Describe the morphology of the red blood cells.
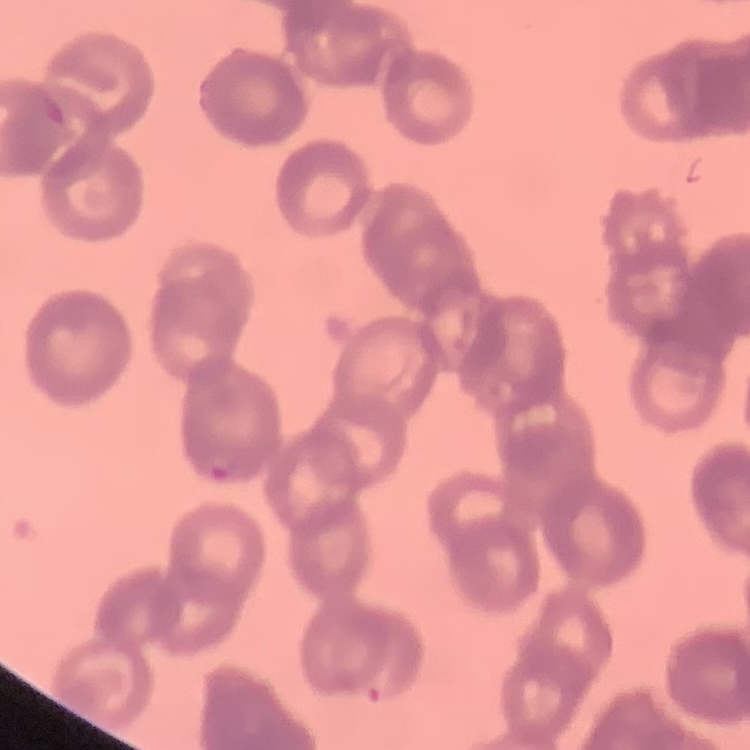

They show rouleaux formation.

preparation = thin blood smear
stain = Field's or Giemsa
image type = one tile cut from a larger photomicrograph